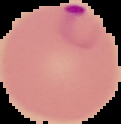

{
  "malaria_status": "parasitized",
  "image_type": "segmented cell region with the area outside set to black",
  "preparation": "thin blood smear",
  "image_size": "121×124 pixels"
}